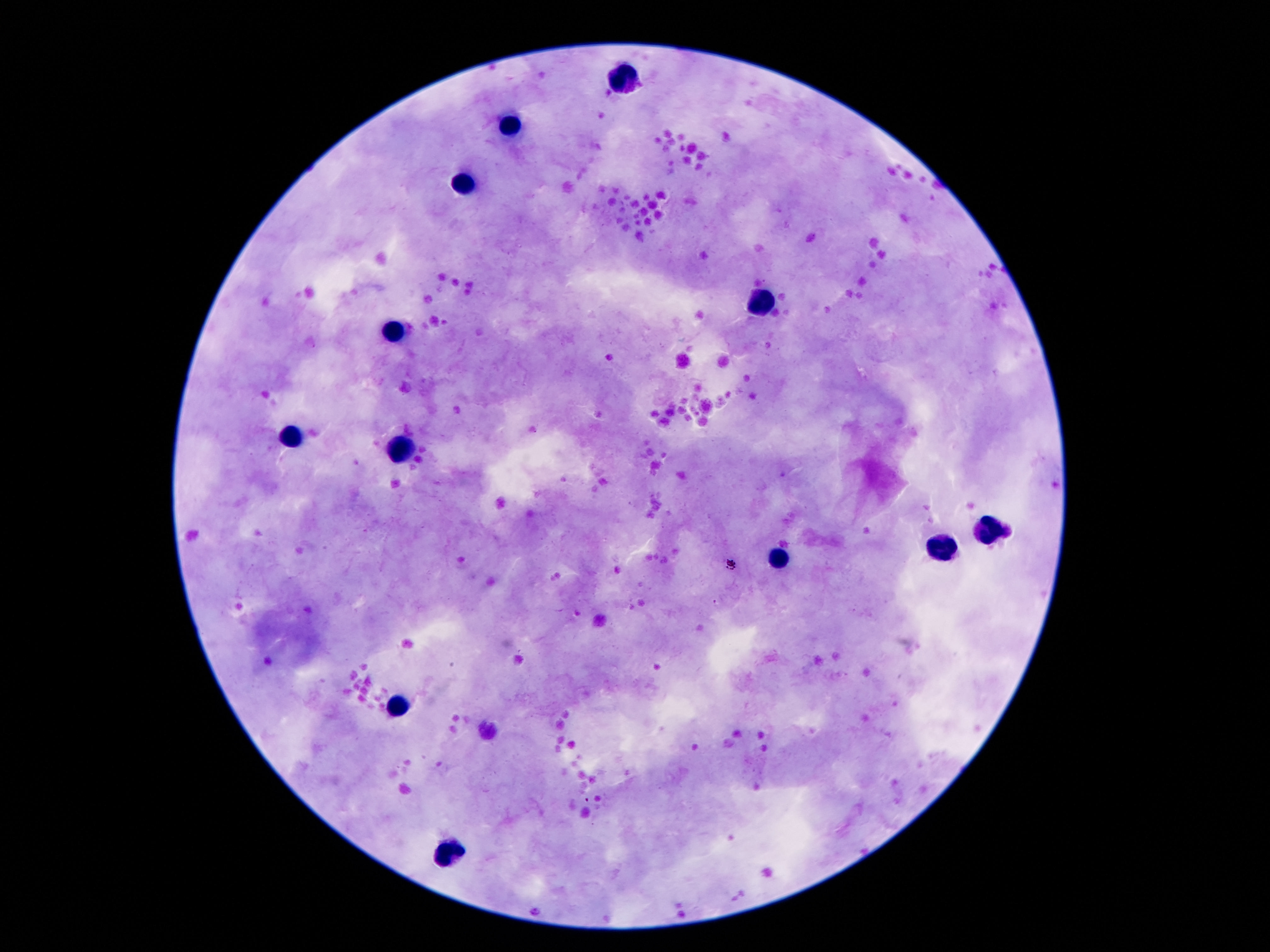 Approximate centers as (x, y) in pixels. Leukocyte locations: (621, 77), (510, 123), (466, 184), (759, 301), (394, 333), (291, 432), (402, 449), (988, 529), (942, 548), (780, 560), (396, 705), (453, 852). Thick peripheral-blood smear. Photographed through the microscope eyepiece with a smartphone camera. Giemsa stain. Single field of view. Image is 1270×952 pixels. 100x magnification. Patient malaria status: negative.